Assess this cell for malaria.
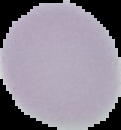

Uninfected.

From a thin blood smear. The area outside the segmented cell region is set to black. Image is 121×130 pixels.